Outline each uninfected red blood cell.
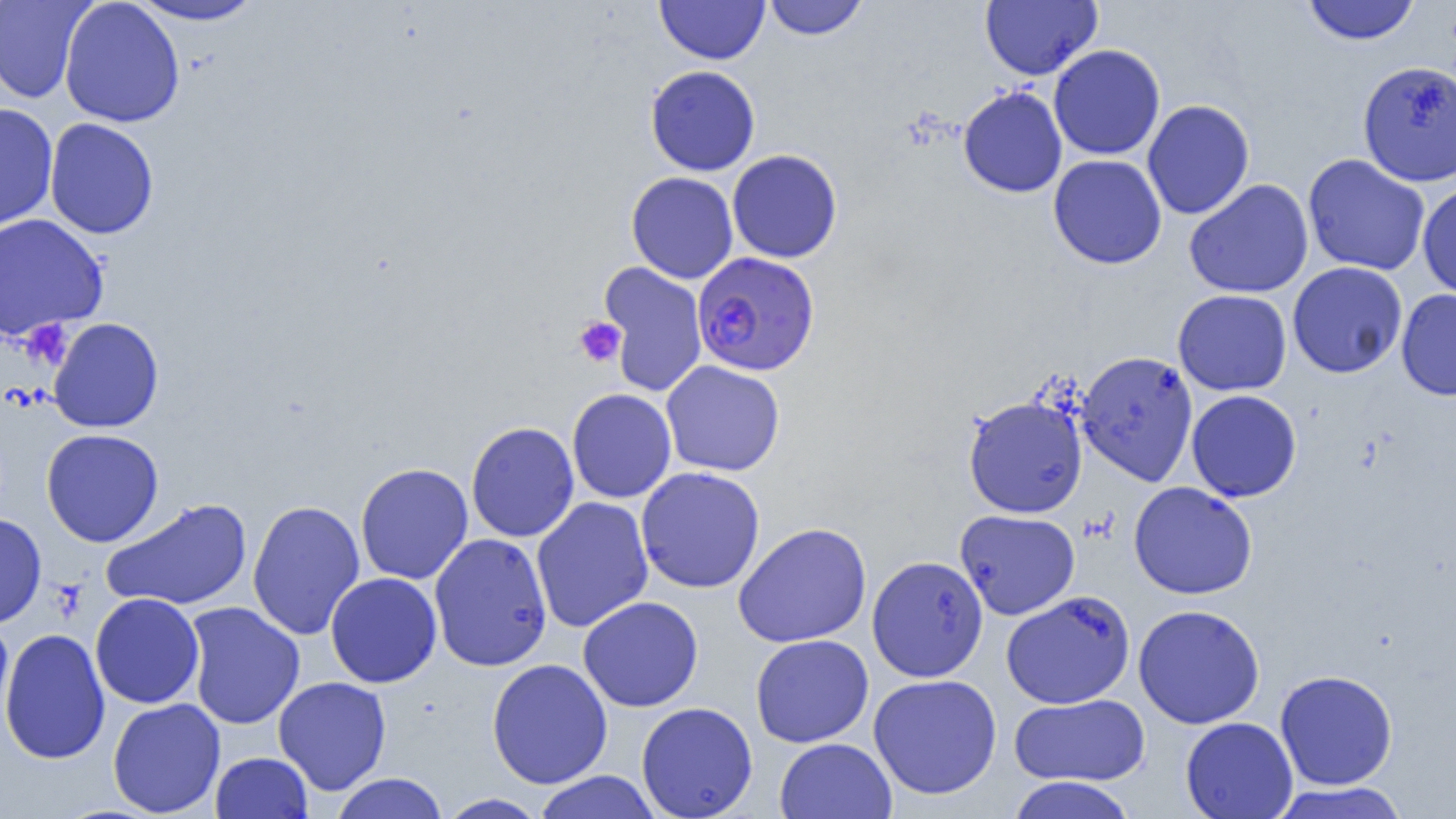

Approximate bounding boxes as (x1, y1, x2, y2) in pixels.
Uninfected red blood cells: (0, 0, 94, 104), (59, 0, 185, 128), (655, 0, 770, 65), (763, 0, 868, 40), (980, 0, 1103, 81), (1302, 0, 1420, 45), (128, 1, 267, 26), (1048, 44, 1165, 160), (1357, 60, 1456, 186), (645, 65, 761, 176), (958, 86, 1068, 198), (1142, 100, 1254, 220), (0, 102, 58, 233), (44, 117, 159, 240), (727, 149, 843, 263), (1048, 154, 1167, 269), (1303, 154, 1430, 276), (626, 172, 738, 283), (1184, 179, 1313, 298), (1417, 182, 1456, 302), (0, 213, 108, 340), (598, 261, 708, 397), (1287, 261, 1408, 379), (1173, 289, 1292, 396), (1396, 290, 1456, 401), (48, 317, 164, 433), (1076, 351, 1198, 486), (661, 360, 786, 477), (567, 388, 677, 503), (1186, 390, 1302, 502), (963, 396, 1088, 518), (466, 421, 579, 542), (41, 428, 164, 547), (355, 462, 473, 585), (635, 466, 765, 593), (1129, 482, 1258, 599), (531, 497, 654, 633), (100, 498, 252, 611), (247, 499, 365, 641), (955, 509, 1080, 620), (0, 513, 47, 628), (732, 522, 872, 647), (429, 533, 552, 672), (867, 555, 988, 682), (325, 572, 442, 688), (1001, 591, 1133, 709), (90, 592, 204, 709), (578, 595, 703, 712), (185, 601, 305, 730), (1133, 604, 1265, 729), (0, 618, 14, 735), (0, 628, 110, 764), (750, 634, 874, 748), (486, 658, 613, 788), (1275, 669, 1398, 790), (868, 673, 1002, 800), (273, 676, 391, 795), (1009, 693, 1149, 786), (107, 698, 226, 818), (636, 702, 757, 819), (1180, 716, 1298, 819), (774, 737, 897, 818), (211, 751, 313, 818), (534, 771, 662, 819), (330, 772, 449, 819), (1006, 776, 1137, 819), (1268, 782, 1412, 819), (436, 793, 548, 818).

Summary:
  - Platelet locations: (574, 317, 627, 367), (20, 320, 73, 370)
  - Plasmodium falciparum-infected red blood cell locations: (692, 252, 820, 376)
  - Slide-level diagnosis: Plasmodium falciparum
  - Modality: optical microscopy
  - Preparation: thin blood smear
  - Magnification: 1000x
  - Image size: 1456×819 pixels
  - Field of view: single